Name the parasite shown.
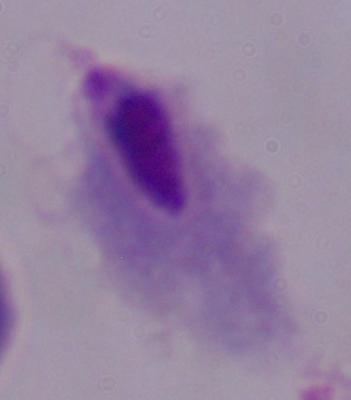

A trichomonad.

Summary:
  - Modality: micrograph
  - Magnification: 1000x